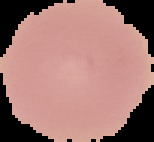

{
  "preparation": "thin blood smear",
  "image_type": "segmented cell region on a black background",
  "malaria_status": "uninfected",
  "image_size": "154×142 pixels"
}